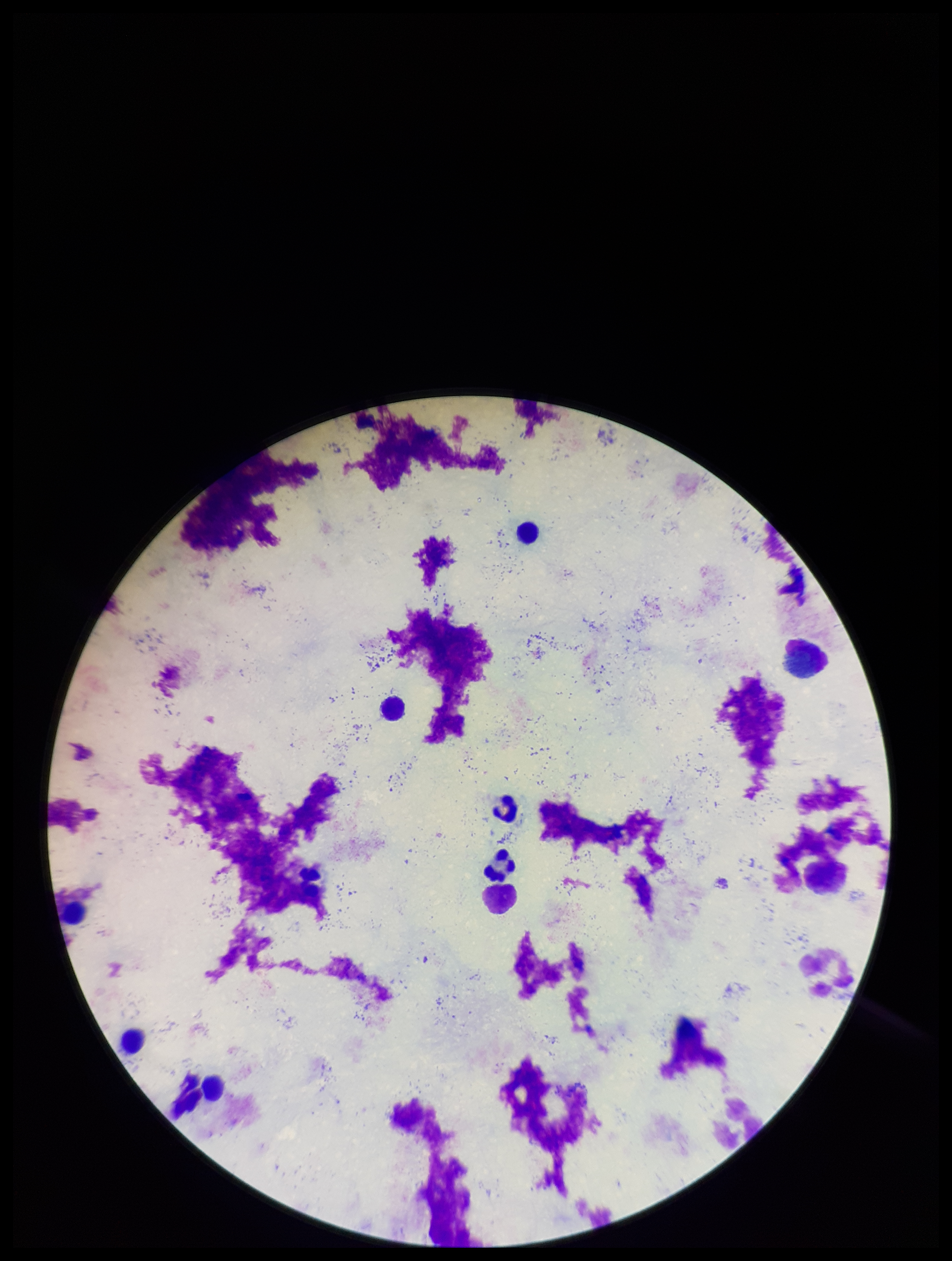
Patient malaria status: negative. Plasmodium parasites: none seen. Parasite count: 0. Smartphone photograph taken through the eyepiece of a microscope. Giemsa stain. Preparation: thick smear. Single field of view. Leukocyte count: 9. Image is 952×1261 pixels.